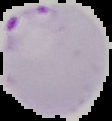

image type = segmented cell region with the area outside set to black
image size = 112×121 pixels
result = malaria parasites identified
preparation = thin blood film